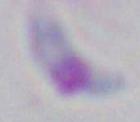 Toxoplasma gondii is shown. 1000x magnification. Photomicrograph.